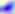
modality = micrograph
magnification = 400x
identification = Toxoplasma gondii